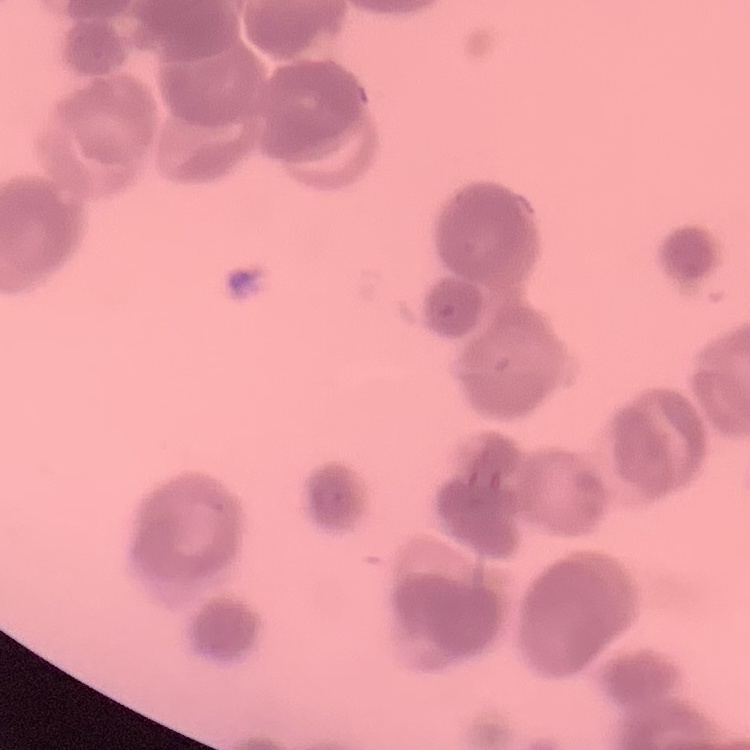

Summary:
  - Erythrocyte morphology: rouleaux formation
  - Stain: Field's or Giemsa
  - Image type: square crop of a larger photomicrograph
  - Preparation: thin blood film